Report the malaria status of this cell.
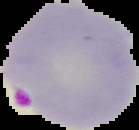
It is parasitized.

The area outside the segmented cell region is set to black. From a thin blood film. Image is 139×130 pixels.